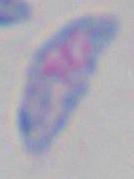

Micrograph. 1000x magnification. Toxoplasma gondii is shown.